State which cell type is depicted.
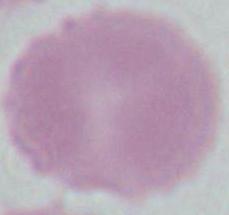

An erythrocyte.

Summary:
  - Magnification: 1000x
  - Modality: photomicrograph